Report the malaria status of this cell.
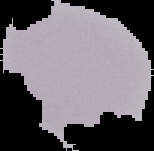

It is uninfected.

{
  "image_type": "cell region segmented out of the field of view; surrounding area masked to black",
  "image_size": "154×151 pixels",
  "preparation": "thin blood smear"
}